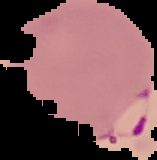

Summary:
  - Malaria status: parasitized
  - Image type: cell region segmented out of the field of view; surrounding area masked to black
  - Preparation: thin blood smear
  - Image size: 157×160 pixels